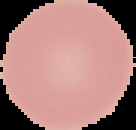

Summary:
  - Preparation: thin blood smear
  - Image size: 136×130 pixels
  - Image type: segmented cell region on a black background
  - Malaria status: uninfected